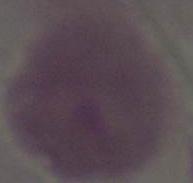

Summary:
  - Modality: photomicrograph
  - Identification: red blood cell
  - Magnification: 1000x